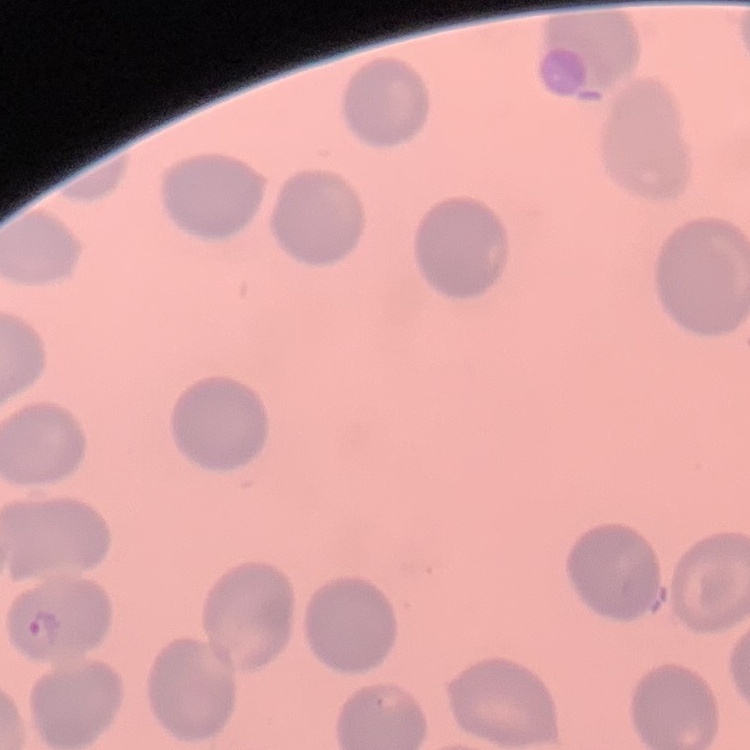

red blood cell morphology = no rouleaux formation
preparation = thin peripheral smear
image type = square crop of a larger photomicrograph
stain = Field's or Giemsa